Outline each Plasmodium falciparum-infected red blood cell.
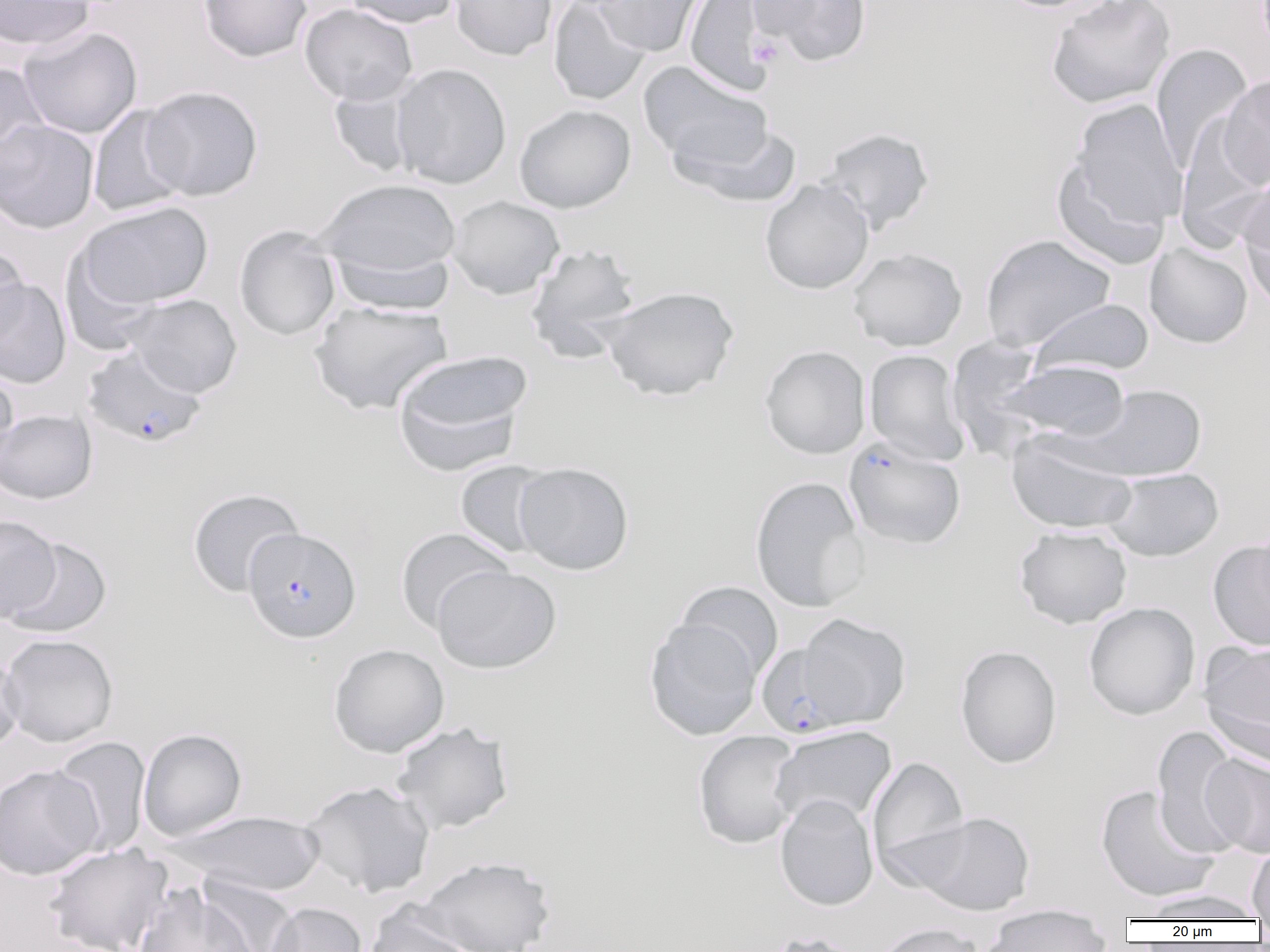

Approximate bounding boxes as (x1, y1, x2, y2) in pixels.
Plasmodium falciparum-infected red blood cells: (82, 345, 206, 449), (843, 437, 966, 550), (242, 527, 361, 643), (756, 642, 856, 737).

Platelet locations: (748, 35, 783, 68). Uninfected red blood cell locations: (0, 0, 95, 51), (198, 0, 311, 62), (342, 0, 460, 28), (449, 0, 557, 61), (548, 0, 651, 106), (593, 0, 708, 57), (684, 0, 775, 95), (751, 0, 874, 67), (993, 0, 1120, 13), (1045, 0, 1176, 110), (299, 3, 418, 106), (18, 25, 142, 139), (1151, 43, 1252, 172), (639, 61, 773, 170), (0, 62, 50, 171), (390, 63, 512, 189), (1216, 74, 1270, 190), (328, 82, 421, 178), (140, 86, 263, 201), (1070, 97, 1188, 232), (88, 104, 189, 218), (514, 104, 636, 213), (1175, 115, 1269, 251), (0, 119, 99, 234), (670, 121, 804, 208), (816, 127, 934, 235), (1051, 155, 1172, 270), (1238, 171, 1270, 304), (315, 178, 461, 277), (760, 179, 874, 295), (446, 195, 565, 299), (77, 201, 213, 309), (234, 226, 341, 341), (980, 234, 1116, 351), (1145, 242, 1252, 348), (524, 243, 643, 361), (0, 244, 29, 349), (328, 245, 456, 315), (847, 247, 967, 352), (60, 248, 165, 356), (0, 279, 72, 388), (600, 285, 739, 401), (123, 294, 242, 398), (1028, 298, 1155, 379), (308, 300, 454, 416), (947, 335, 1049, 458), (760, 345, 870, 459), (392, 349, 532, 473), (864, 349, 970, 465), (999, 360, 1130, 442), (0, 367, 19, 471), (1074, 384, 1206, 481), (0, 408, 97, 504), (1006, 431, 1137, 534), (454, 460, 557, 558), (513, 462, 634, 575), (1103, 468, 1224, 562), (749, 476, 869, 612), (187, 488, 305, 597), (0, 515, 61, 622), (1014, 525, 1132, 629), (394, 527, 514, 633), (2, 535, 112, 639), (1207, 539, 1270, 651), (431, 565, 561, 674), (675, 581, 784, 681), (1083, 602, 1200, 720), (796, 613, 911, 728), (643, 617, 763, 740), (0, 634, 118, 748), (1199, 639, 1270, 759), (328, 643, 449, 758), (955, 645, 1062, 768), (0, 647, 24, 755), (390, 721, 514, 835), (1152, 725, 1248, 859), (770, 726, 897, 829), (138, 728, 247, 841), (692, 731, 804, 849), (50, 736, 151, 856), (1201, 754, 1270, 859), (867, 755, 969, 879), (0, 764, 103, 880), (302, 780, 435, 898), (1095, 785, 1219, 903), (774, 794, 878, 911), (171, 810, 328, 897), (909, 812, 1035, 916), (44, 843, 173, 952), (1247, 843, 1270, 921), (416, 855, 556, 952), (196, 875, 301, 952), (133, 884, 259, 952), (1139, 889, 1267, 921), (266, 902, 367, 952), (363, 903, 480, 952), (981, 909, 1113, 951), (872, 922, 986, 952), (756, 930, 870, 952). Slide-level diagnosis: Plasmodium falciparum. One field of a larger specimen. Image is 1270×952 pixels. 1000x magnification. Optical microscopy. Thin blood film.